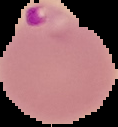

preparation = thin blood smear
malaria status = parasitized
image size = 118×127 pixels
image type = segmented cell region on a black background